Report the malaria status of this cell.
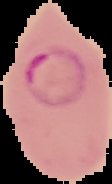
It is parasitized.

Summary:
  - Image type: cell region segmented out of the field of view; surrounding area masked to black
  - Preparation: thin blood smear
  - Image size: 112×184 pixels